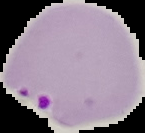

image size = 145×133 pixels
preparation = thin blood film
malaria status = parasitized
image type = segmented cell region on a black background